Draw a bounding box around every leukocyte (white blood cell).
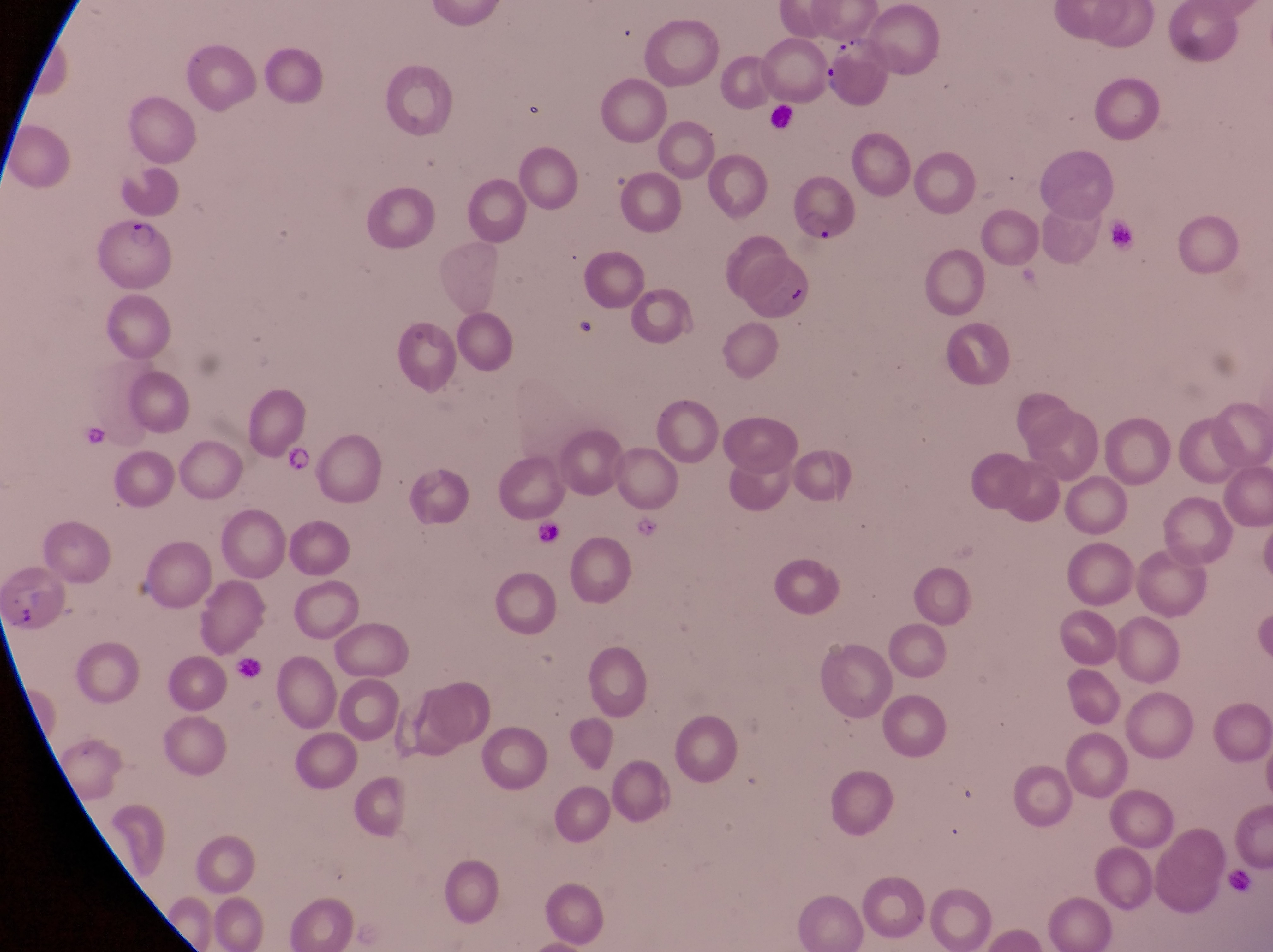
No leukocytes observed.

Approximate bounding boxes as {left, top, right, bottom} in pixels. Trophozoite locations: {817, 63, 842, 96}, {278, 449, 317, 477}. Artifact (platelet-like body, stain precipitate, or debris) locations: {778, 282, 808, 312}, {571, 318, 616, 358}, {10, 600, 47, 637}. Parasitised red blood cell locations: {88, 222, 185, 294}. Single field of view. Thin blood film. Photographed through the eyepiece of an Olympus CX-23 microscope with a smartphone camera. Collected in Uganda. At a magnification of 1000x. Image is 1273×952 pixels.